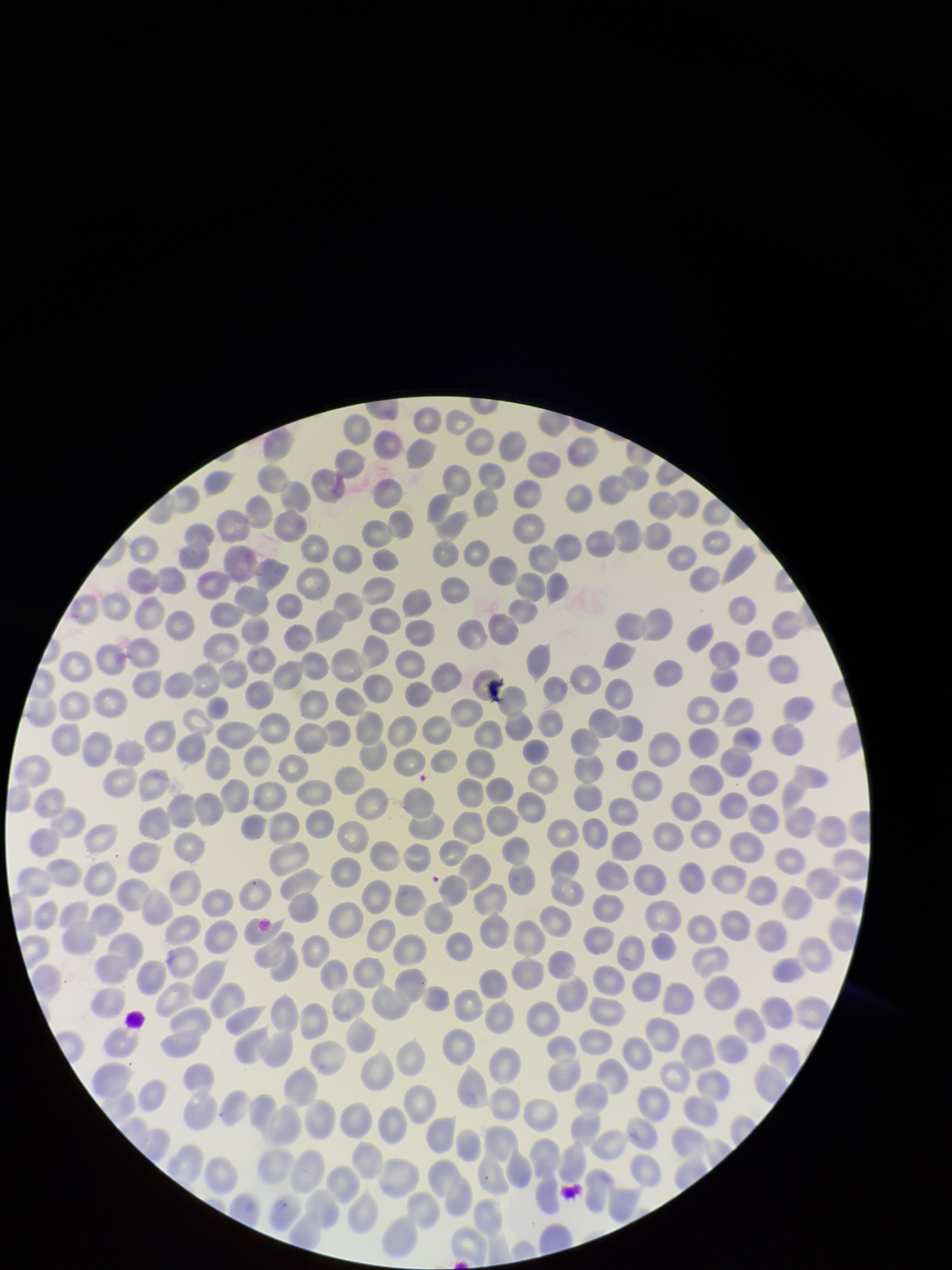
Summary:
  - Capture: smartphone photograph through the microscope eyepiece
  - Patient malaria status: positive
  - Parasitized red blood cells: none detected
  - Preparation: thin smear
  - Species reported for this patient: Plasmodium falciparum
  - Image size: 952×1270 pixels
  - Field of view: one from this slide
  - Stain: Giemsa
  - Parasitized red blood cell count: 0
  - Red blood cell count: 350